Outline each white blood cell.
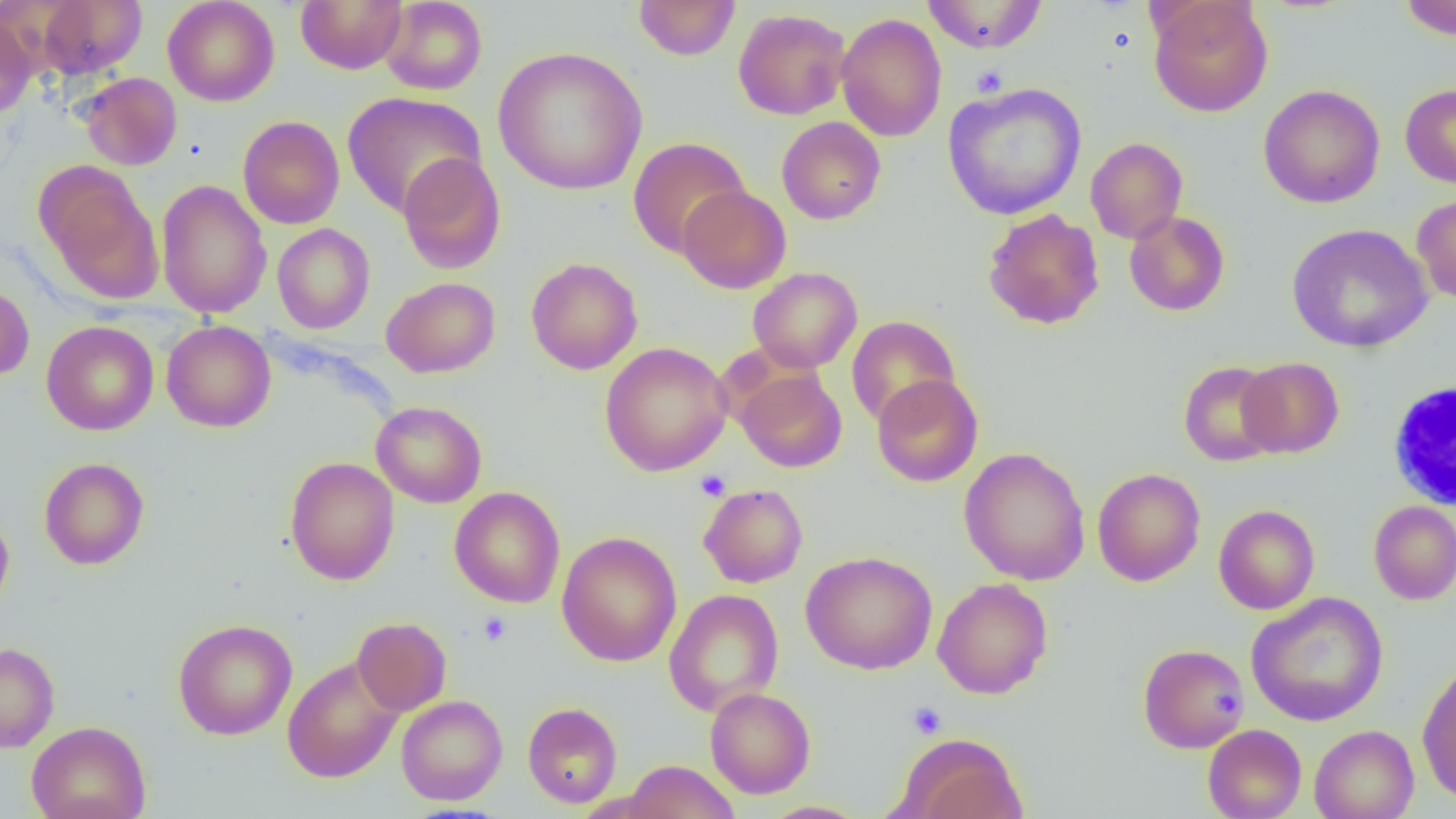
Approximate bounding boxes as [x1, y1, x2, y2] in pixels.
White blood cells: [1385, 377, 1455, 513].

Summary:
  - Platelet locations: [970, 65, 1008, 97], [695, 470, 731, 501], [478, 612, 512, 646], [907, 701, 947, 739]
  - Uninfected red blood cell locations: [35, 0, 147, 79], [162, 0, 280, 106], [296, 0, 407, 74], [633, 0, 741, 61], [921, 0, 1048, 54], [1399, 0, 1456, 40], [380, 1, 487, 95], [1148, 1, 1273, 117], [733, 8, 851, 120], [0, 12, 36, 119], [835, 12, 947, 142], [493, 46, 649, 195], [79, 72, 182, 170], [942, 82, 1087, 220], [1400, 83, 1456, 189], [1258, 84, 1385, 208], [342, 92, 486, 217], [238, 116, 344, 228], [776, 116, 886, 224], [627, 137, 750, 258], [1085, 137, 1187, 244], [397, 152, 506, 274], [36, 162, 164, 301], [156, 180, 272, 318], [677, 185, 791, 293], [1412, 193, 1456, 306], [983, 208, 1104, 329], [1124, 211, 1230, 316], [272, 223, 375, 334], [1286, 224, 1433, 352], [526, 257, 643, 375], [748, 267, 862, 373], [381, 276, 500, 378], [0, 282, 35, 381], [846, 315, 961, 428], [41, 320, 158, 435], [161, 320, 276, 432], [599, 341, 733, 476], [1237, 357, 1344, 458], [1178, 360, 1283, 466], [734, 367, 847, 472], [871, 374, 984, 487], [371, 401, 487, 508], [959, 447, 1090, 585], [284, 456, 399, 585], [39, 457, 149, 570], [1092, 467, 1205, 586], [698, 484, 809, 588], [449, 487, 565, 607], [1368, 500, 1456, 605], [1213, 504, 1320, 614], [0, 511, 14, 616], [556, 531, 682, 667], [801, 550, 938, 674], [932, 577, 1053, 699], [664, 589, 784, 716], [1246, 592, 1389, 726], [351, 617, 451, 715], [173, 618, 297, 740], [0, 642, 60, 753], [1138, 643, 1250, 753], [282, 656, 403, 783], [1417, 660, 1456, 805], [705, 687, 815, 798], [396, 695, 507, 805], [523, 702, 622, 808], [26, 721, 151, 819], [1202, 724, 1306, 819], [1309, 725, 1419, 819], [894, 732, 1027, 819], [623, 759, 740, 819], [760, 801, 869, 819]
  - Slide-level diagnosis: negative for blood parasites
  - Modality: optical microscopy
  - Field of view: one of a larger specimen
  - Image size: 1456×819 pixels
  - Preparation: thin blood film
  - Magnification: 1000x